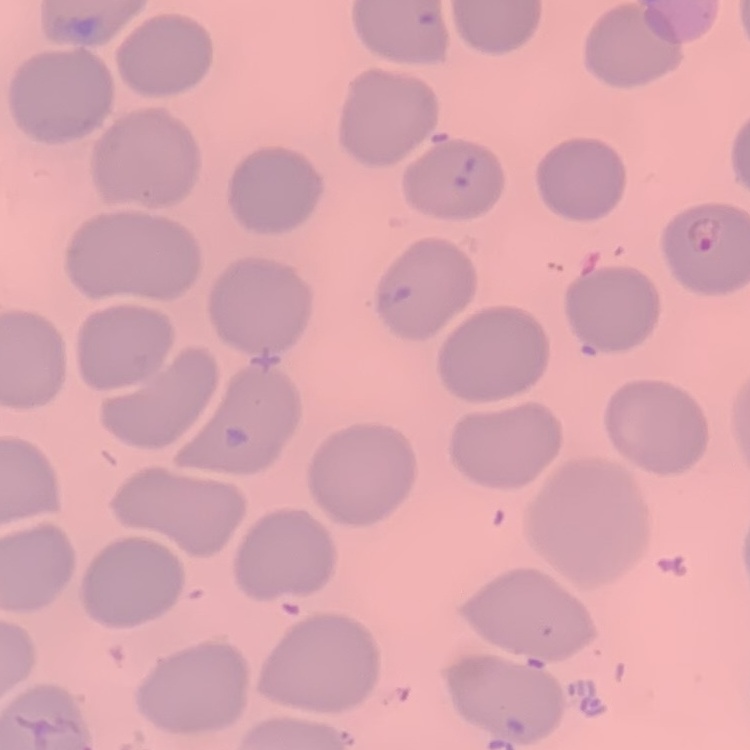

Summary:
  - Red blood cell morphology: no rouleaux formation
  - Stain: Field's or Giemsa
  - Preparation: thin blood film
  - Image type: one tile cut from a larger photomicrograph